Assess this cell for malaria.
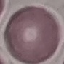

It is uninfected.

Summary:
  - Capture: smartphone through the microscope eyepiece
  - Preparation: thin blood smear
  - Stain: Giemsa
  - Image type: automatically extracted cell patch, resized to 64 × 64 pixels